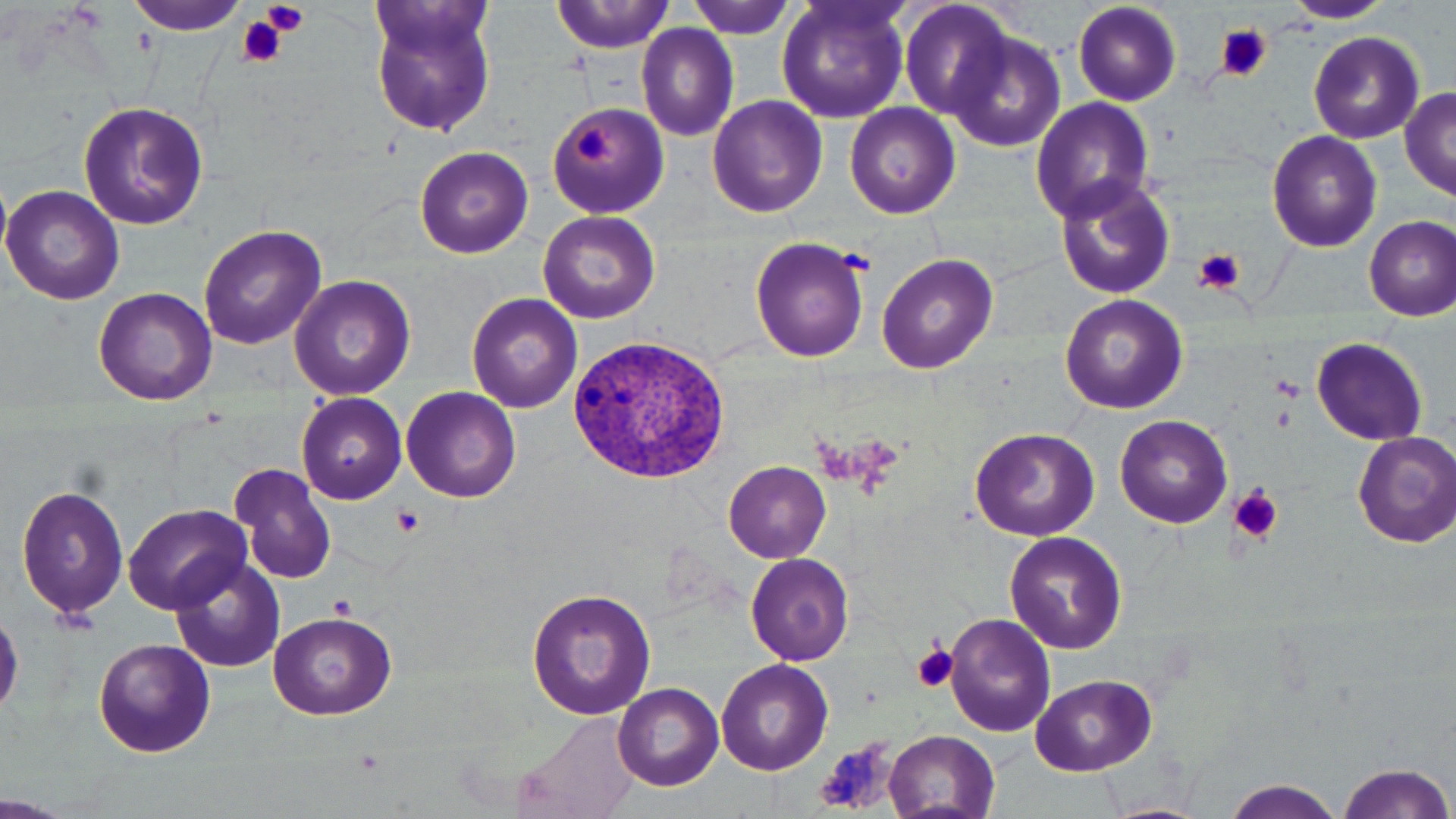
Summary:
  - Coordinate format: approximate bounding boxes as named x1/y1/x2/y2 corners in pixels
  - Uninfected red blood cell locations: (x1=127, y1=0, x2=252, y2=35), (x1=364, y1=0, x2=499, y2=139), (x1=553, y1=0, x2=673, y2=54), (x1=686, y1=0, x2=796, y2=39), (x1=774, y1=0, x2=912, y2=124), (x1=1070, y1=0, x2=1183, y2=107), (x1=899, y1=1, x2=1015, y2=122), (x1=1282, y1=1, x2=1396, y2=23), (x1=636, y1=25, x2=739, y2=142), (x1=945, y1=29, x2=1066, y2=151), (x1=1308, y1=31, x2=1424, y2=143), (x1=1399, y1=87, x2=1456, y2=200), (x1=706, y1=95, x2=828, y2=217), (x1=1029, y1=97, x2=1155, y2=225), (x1=546, y1=100, x2=668, y2=218), (x1=80, y1=101, x2=205, y2=230), (x1=844, y1=103, x2=959, y2=218), (x1=1266, y1=131, x2=1382, y2=253), (x1=413, y1=145, x2=534, y2=258), (x1=1053, y1=175, x2=1176, y2=301), (x1=0, y1=184, x2=126, y2=305), (x1=537, y1=210, x2=660, y2=324), (x1=1363, y1=215, x2=1456, y2=320), (x1=198, y1=225, x2=328, y2=351), (x1=748, y1=236, x2=870, y2=362), (x1=878, y1=252, x2=997, y2=374), (x1=289, y1=274, x2=416, y2=402), (x1=92, y1=286, x2=218, y2=406), (x1=466, y1=293, x2=582, y2=412), (x1=1059, y1=294, x2=1187, y2=413), (x1=1310, y1=336, x2=1428, y2=444), (x1=402, y1=387, x2=521, y2=502), (x1=296, y1=392, x2=407, y2=504), (x1=1116, y1=414, x2=1233, y2=529), (x1=970, y1=427, x2=1099, y2=542), (x1=1352, y1=431, x2=1456, y2=547), (x1=724, y1=462, x2=830, y2=561), (x1=231, y1=464, x2=336, y2=585), (x1=16, y1=483, x2=130, y2=622), (x1=125, y1=505, x2=254, y2=614), (x1=1004, y1=531, x2=1127, y2=655), (x1=745, y1=551, x2=857, y2=665), (x1=168, y1=557, x2=287, y2=673), (x1=525, y1=585, x2=656, y2=722), (x1=266, y1=610, x2=398, y2=720), (x1=944, y1=611, x2=1054, y2=737), (x1=91, y1=638, x2=217, y2=758), (x1=716, y1=659, x2=832, y2=775), (x1=1030, y1=673, x2=1156, y2=775), (x1=613, y1=683, x2=724, y2=790), (x1=509, y1=712, x2=640, y2=819), (x1=883, y1=730, x2=1001, y2=817), (x1=1334, y1=761, x2=1453, y2=819), (x1=1223, y1=779, x2=1346, y2=819)
  - Platelet locations: (x1=262, y1=0, x2=310, y2=34), (x1=236, y1=16, x2=288, y2=68), (x1=1216, y1=25, x2=1270, y2=82), (x1=574, y1=126, x2=618, y2=167), (x1=1191, y1=247, x2=1248, y2=297), (x1=1229, y1=484, x2=1283, y2=543), (x1=391, y1=505, x2=424, y2=538), (x1=330, y1=595, x2=356, y2=620), (x1=911, y1=643, x2=959, y2=694), (x1=814, y1=738, x2=900, y2=813)
  - Plasmodium vivax-infected red blood cell locations: (x1=564, y1=333, x2=735, y2=487)
  - Slide-level diagnosis: Plasmodium vivax
  - Stain: May-Grünwald-Giemsa
  - Preparation: thin blood film
  - Field of view: single
  - Magnification: 1000x
  - Image size: 1456×819 pixels
  - Modality: optical microscopy